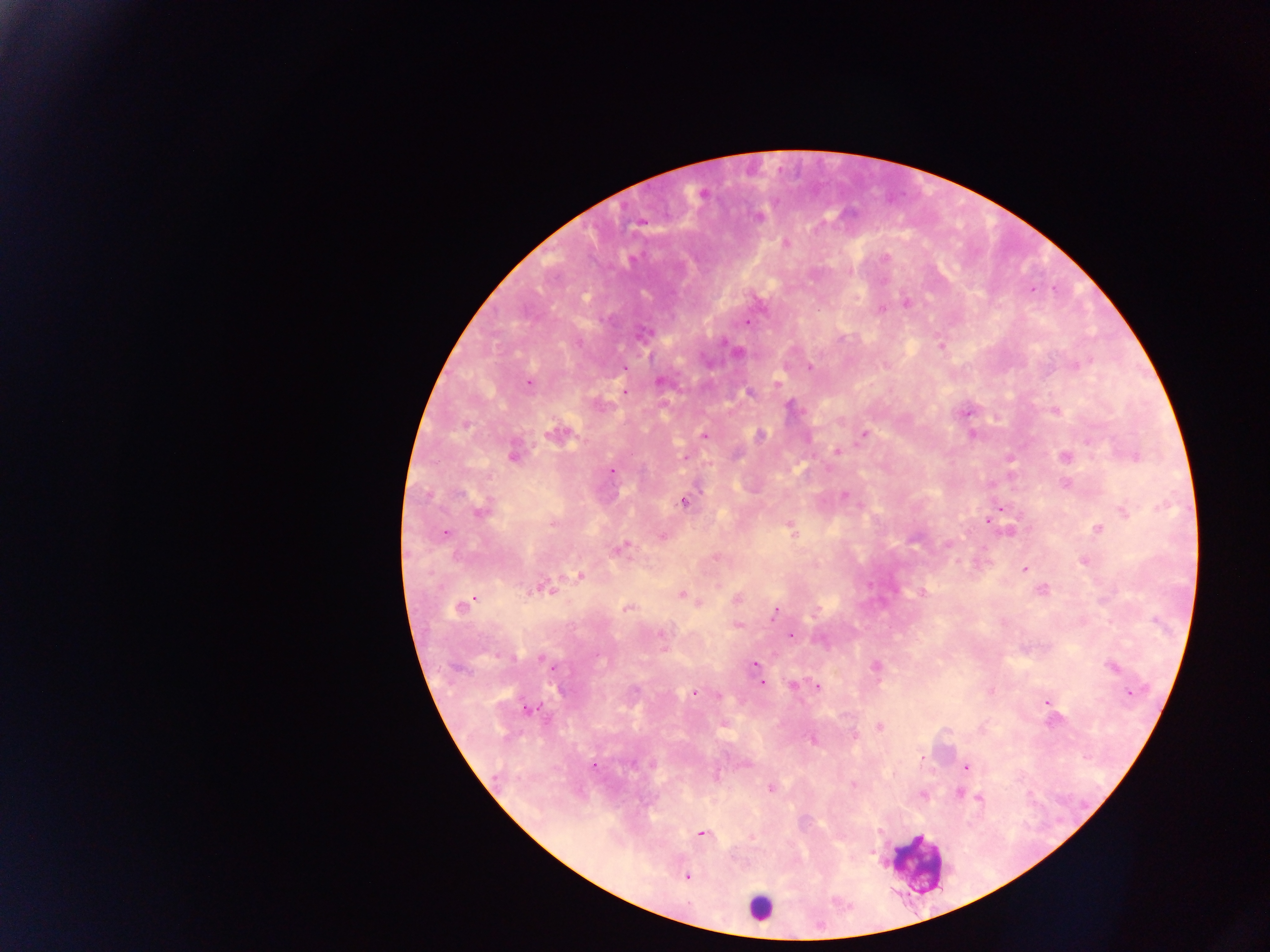

Approximate centers as {x, y} in pixels.
Summary:
  - Leukocyte locations: {759, 908}
  - Malaria parasite locations: {702, 195}, {757, 217}, {640, 222}, {785, 242}, {1031, 289}, {906, 302}, {881, 308}, {747, 322}, {643, 335}, {940, 345}, {737, 352}, {1074, 365}, {623, 368}, {810, 368}, {661, 381}, {528, 382}, {776, 385}, {623, 391}, {749, 393}, {791, 407}, {1054, 410}, {965, 413}, {557, 432}, {864, 433}, {761, 435}, {972, 435}, {703, 436}, {836, 450}, {513, 453}, {1134, 455}, {1065, 456}, {1009, 459}, {611, 471}, {1066, 483}, {845, 495}, {683, 501}, {1001, 507}, {481, 509}, {1125, 510}, {988, 518}, {553, 523}, {791, 528}, {1097, 529}, {1010, 531}, {445, 533}, {662, 535}, {948, 545}, {620, 548}, {716, 556}, {1083, 560}, {1024, 569}, {579, 575}, {541, 588}, {1042, 591}, {922, 592}, {681, 595}, {472, 597}, {735, 599}, {698, 602}, {460, 607}, {628, 607}, {775, 612}, {737, 625}, {790, 635}, {755, 664}, {875, 666}, {1112, 667}, {757, 672}, {761, 682}, {793, 685}, {817, 686}, {1128, 691}, {693, 692}, {1046, 701}, {530, 708}, {723, 724}, {878, 726}, {853, 736}, {812, 740}, {745, 763}, {594, 765}, {965, 767}, {853, 784}, {770, 788}, {957, 792}, {980, 798}, {700, 833}, {751, 836}, {686, 876}
  - Preparation: thick blood smear
  - Image size: 1270×952 pixels
  - Capture: mobile-phone photograph through a microscope
  - Country: Ghana
  - Field of view: single